Report the malaria status of this cell.
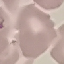

Uninfected.

capture = smartphone through the microscope eyepiece
image type = cell patch, automatically extracted from a larger field of view and resized to 64 × 64 pixels
preparation = thin blood film
stain = Giemsa